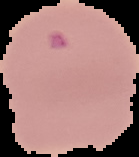

From a thin blood smear. Cell region segmented out of the field of view; the surrounding area is masked to black. Malaria status: parasitized. Image is 139×157 pixels.